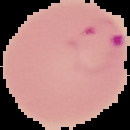

image_type: segmented cell region with the area outside set to black
preparation: thin blood film
malaria_status: parasitized
image_size: 130×130 pixels